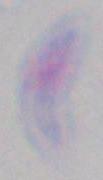
identification: Toxoplasma gondii
modality: photomicrograph
magnification: 1000x